Assess this cell for malaria.
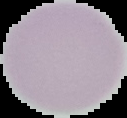
It is uninfected.

Image is 127×118 pixels. Segmented cell region on a black background. From a thin blood film.